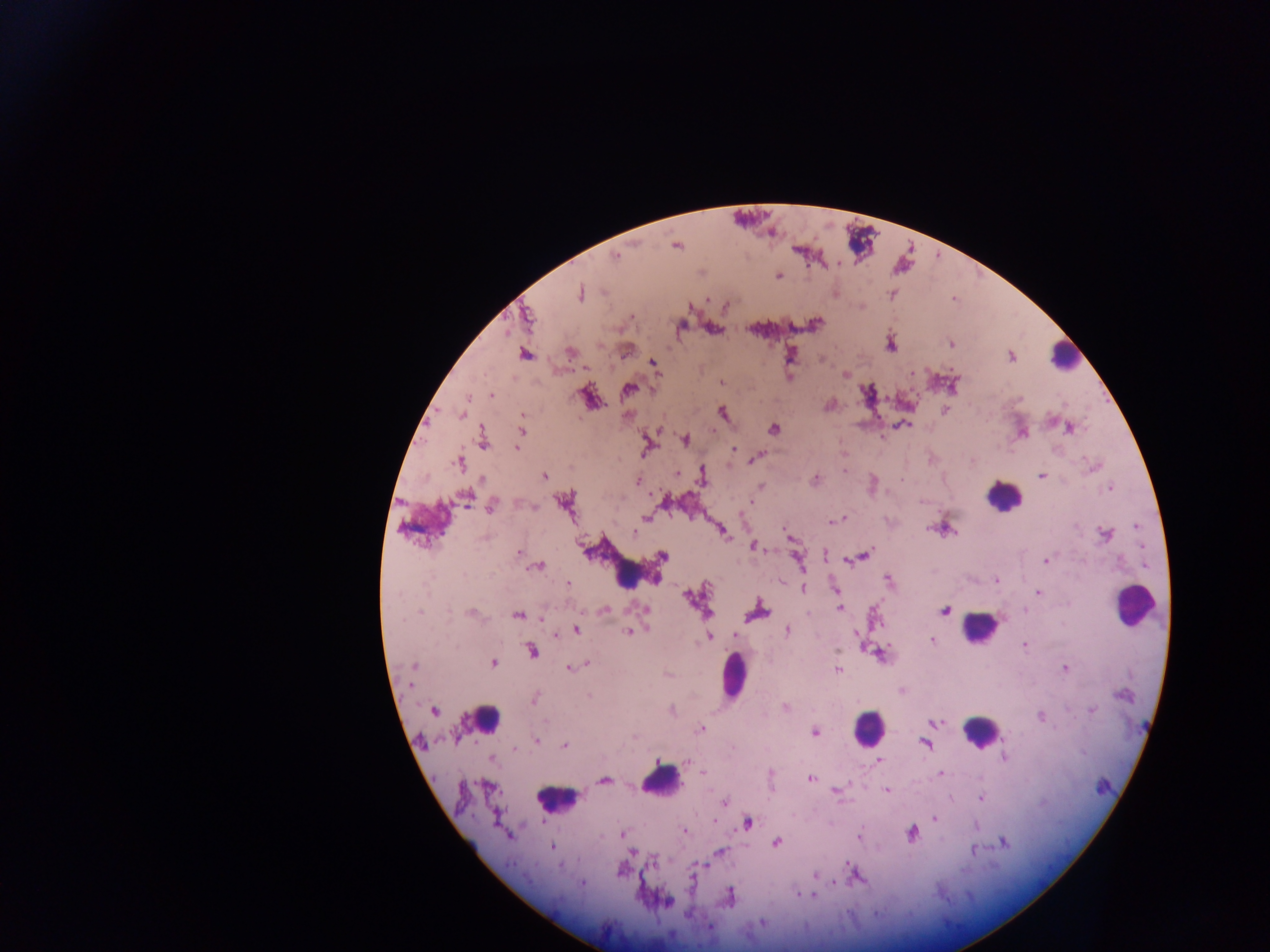

Approximate centers as x y in pixels. Leukocyte locations: 1063 355; 1000 498; 627 574; 1138 609; 979 625; 734 669; 487 721; 868 726; 982 732; 660 781; 558 798. Plasmodium parasite locations: 677 247; 616 256; 780 277; 579 294; 631 316; 530 317; 682 326; 950 344; 569 353; 525 354; 1011 357; 654 362; 844 374; 720 383; 628 389; 491 394; 469 397; 830 405; 462 414; 659 429; 1069 429; 522 433; 517 449; 734 449; 758 455; 970 459; 1084 460; 844 471; 677 472; 1041 475; 544 477; 480 481; 638 481; 1109 487; 661 495; 664 500; 922 501; 519 504; 492 510; 844 517; 646 518; 828 522; 930 525; 1136 528; 950 529; 722 531; 636 534; 788 534; 486 536; 1103 536; 750 545; 517 550; 767 551; 825 552; 867 555; 849 559; 1045 560; 798 561; 541 567; 535 568; 888 578; 995 580; 997 583; 567 584; 803 587; 705 589; 1037 592; 686 597; 641 608; 839 609; 1026 610; 603 611; 945 611; 419 613; 875 613; 449 614; 710 614; 472 615; 808 615; 543 621; 575 630; 788 630; 635 632; 857 633; 732 634; 556 637; 713 638; 708 639; 931 639; 836 651; 494 662; 587 663; 415 666; 1066 668; 570 670; 838 672; 412 685; 589 694; 535 701; 1093 709; 433 710; 1040 717; 546 720; 935 722; 701 728; 815 733; 633 736; 1002 738; 538 741; 925 744; 564 746; 1005 756; 878 759; 657 764; 703 773; 940 773; 811 778; 603 779; 885 790; 836 791; 980 798; 724 802; 934 819; 714 821; 749 823; 686 831; 912 832; 622 833; 510 834; 860 836; 774 843; 1004 843; 550 846; 718 851; 631 852; 973 852; 849 861; 654 863; 560 867; 815 875; 835 884; 796 894; 813 895; 732 896; 669 901; 762 922; 708 925. Sample from Ghana. Image is 1270×952 pixels. Photographed through a microscope with a mobile-phone camera. One field of view. Thick blood smear.